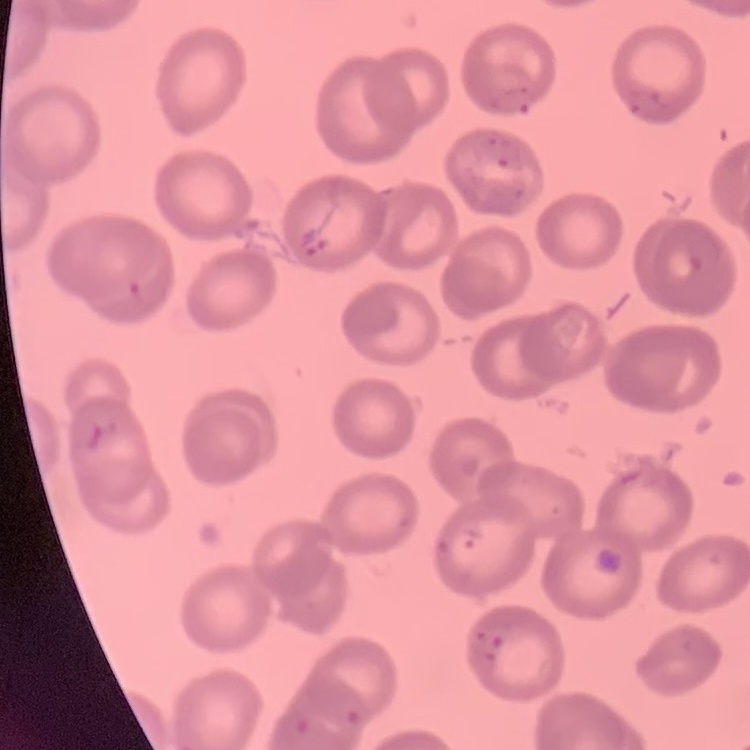
The red blood cells exhibit no rouleaux formation. Thin blood smear. Stained with either Field's or Giemsa. Square crop of a larger photomicrograph.